Assess this cell for malaria.
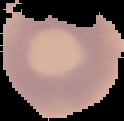
Uninfected.

From a thin blood film. Cell region segmented out of the field of view; the surrounding area is masked to black. Image is 124×121 pixels.